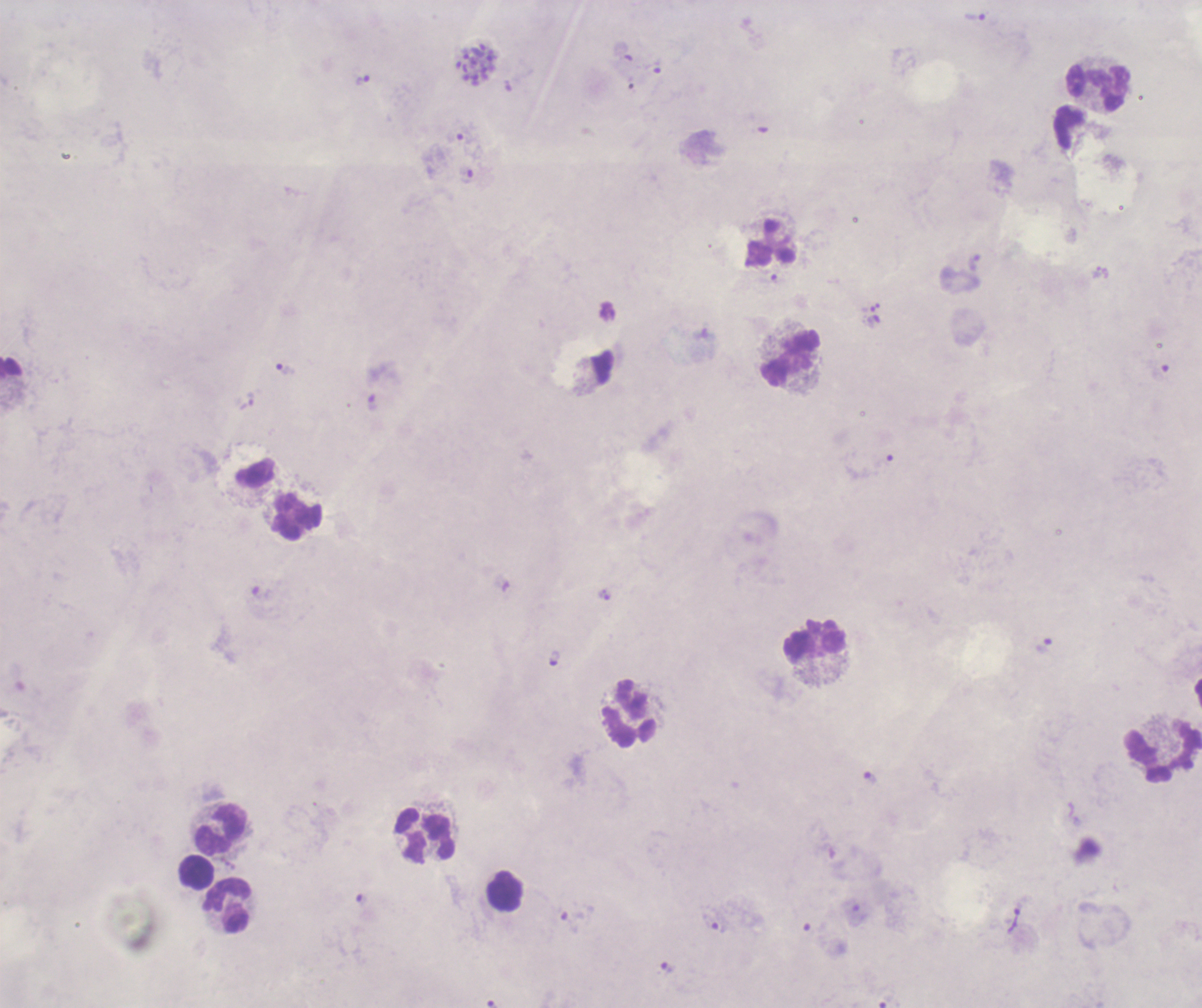

Approximate centers as {x, y} in pixels.
Summary:
  - Leukocyte locations: {1098, 87}, {772, 243}, {790, 358}, {11, 369}, {296, 517}, {814, 639}, {629, 713}, {1163, 753}, {221, 830}, {424, 834}, {196, 872}, {504, 891}, {227, 906}
  - Trophozoite locations: {975, 18}, {363, 80}, {467, 177}, {973, 263}, {769, 280}, {286, 370}, {372, 403}, {1044, 646}, {554, 658}, {870, 777}, {568, 923}, {715, 923}, {667, 969}
  - Schizont locations: {476, 64}
  - Life-cycle stages observed: trophozoite, schizont
  - Field of view: single
  - Context: previously used in a real diagnosis
  - Preparation: thick blood film
  - Magnification: 100x
  - Coloration quality: bad
  - Image size: 1202×1008 pixels
  - Result: malaria parasites detected
  - Background quality: unsatisfactory
  - Stain: Romanowsky